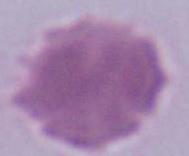

Summary:
  - Identification: erythrocyte
  - Modality: micrograph
  - Magnification: 1000x